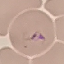

Summary:
  - Result: malaria parasites identified
  - Image type: cell patch, automatically extracted from a larger field of view and resized to 64 × 64 pixels
  - Preparation: thin blood smear
  - Capture: smartphone through the microscope eyepiece
  - Stain: Giemsa